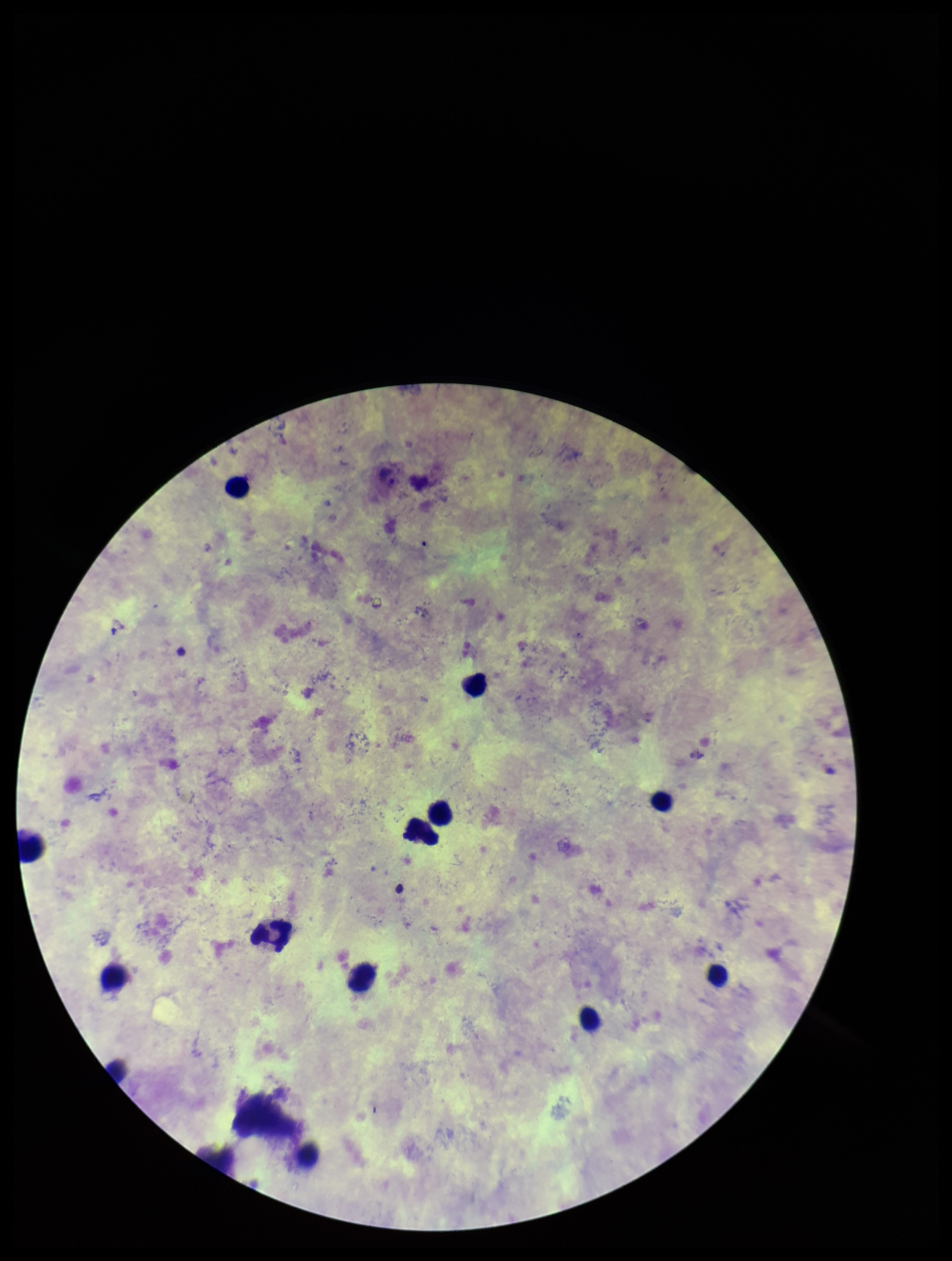
Species reported for this patient: Plasmodium vivax. Leukocyte count: 12. Plasmodium parasites: none identified. Patient malaria status: positive. Preparation: thick. Smartphone photograph taken through the eyepiece of a microscope. One field from this slide. Image is 952×1261 pixels. Parasite count: 0. Stained with Giemsa.